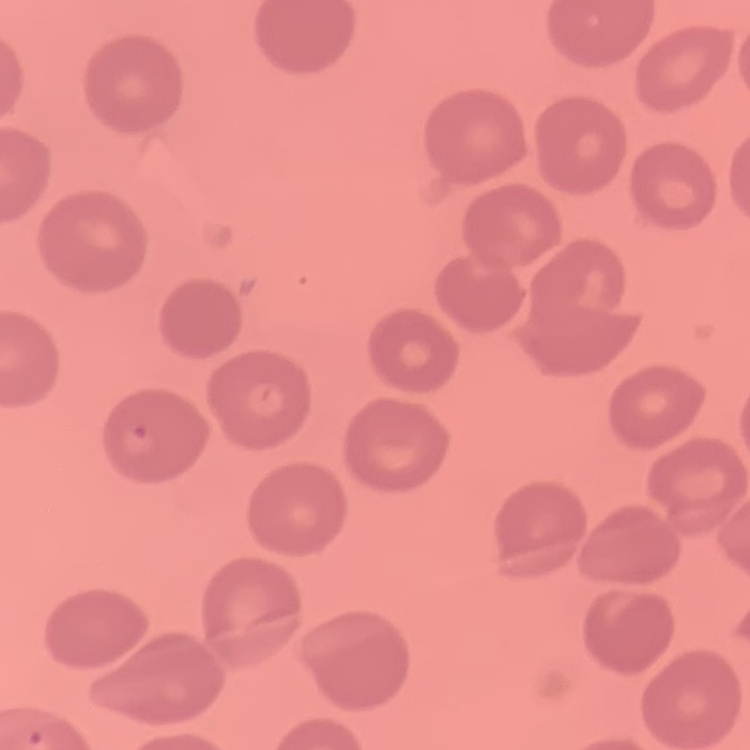

The red blood cells show no rouleaux formation. Field's or Giemsa stain. Thin blood film. Square crop of a larger photomicrograph.